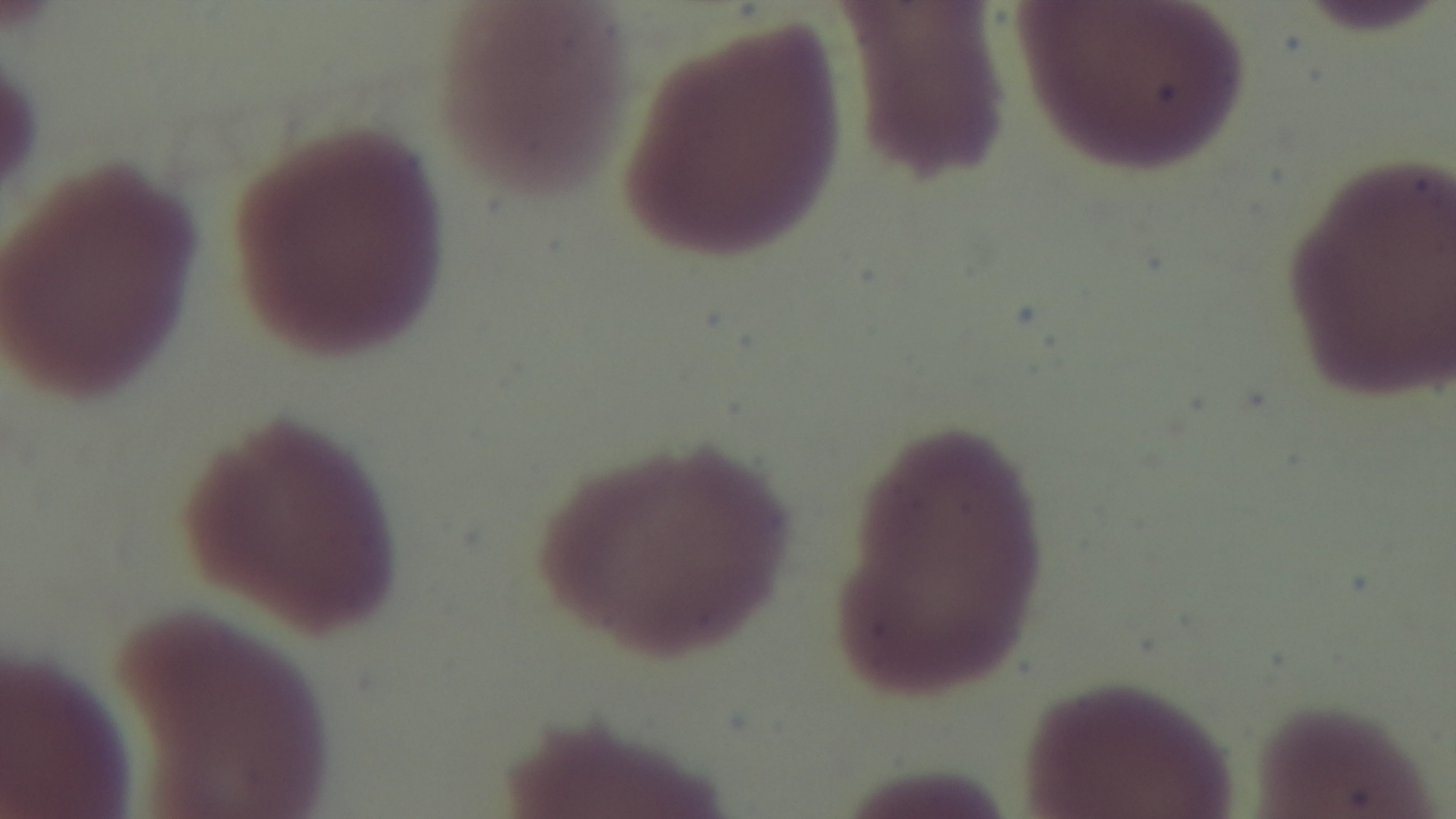 Oil-immersion objective, 100x. Preparation: thin blood film. One field from the slide. Malaria status: uninfected. Giemsa stain. Photomicrograph. Mounted 4K digital camera.